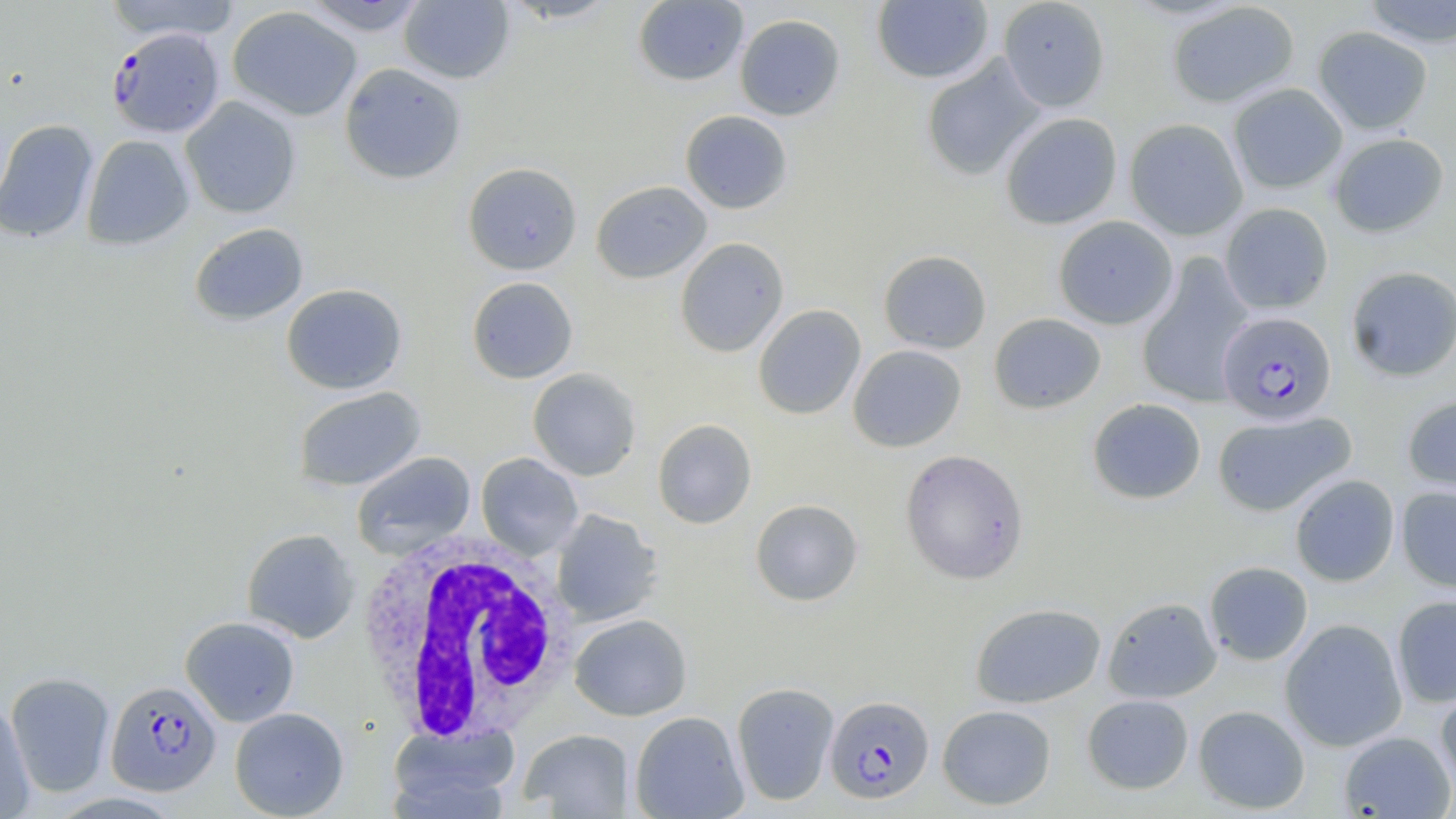
Approximate bounding boxes as (x1, y1, x2, y2) in pixels. Uninfected red blood cell locations: (103, 0, 242, 41), (296, 0, 432, 36), (998, 0, 1111, 112), (399, 1, 514, 85), (500, 1, 621, 24), (632, 1, 748, 87), (872, 1, 994, 84), (1166, 1, 1300, 108), (1359, 1, 1456, 48), (227, 6, 362, 121), (735, 14, 845, 121), (1312, 26, 1433, 134), (920, 54, 1046, 181), (339, 62, 467, 184), (1227, 83, 1347, 195), (180, 96, 302, 219), (679, 110, 793, 214), (999, 112, 1123, 230), (1124, 118, 1248, 240), (0, 119, 98, 243), (1328, 132, 1449, 238), (81, 134, 195, 251), (462, 162, 582, 275), (591, 180, 712, 284), (1220, 203, 1334, 314), (1053, 215, 1178, 330), (189, 222, 308, 326), (674, 237, 789, 357), (878, 250, 992, 354), (1136, 255, 1255, 408), (1345, 266, 1456, 381), (466, 277, 578, 383), (281, 283, 408, 395), (753, 304, 866, 420), (989, 312, 1106, 414), (848, 345, 967, 452), (527, 368, 641, 481), (292, 386, 427, 491), (1402, 394, 1456, 498), (1087, 398, 1206, 504), (1212, 411, 1356, 517), (652, 419, 757, 529), (899, 449, 1029, 585), (351, 451, 476, 559), (476, 453, 583, 559), (1290, 473, 1400, 587), (1396, 486, 1456, 593), (750, 498, 864, 606), (550, 509, 664, 626), (241, 528, 359, 644), (1204, 561, 1313, 666), (1391, 594, 1456, 708), (1102, 597, 1222, 703), (970, 602, 1105, 708), (569, 614, 692, 721), (180, 616, 300, 726), (1280, 618, 1407, 752), (5, 672, 115, 797), (731, 681, 839, 806), (1435, 683, 1456, 794), (1082, 693, 1194, 795), (0, 700, 36, 817), (937, 705, 1057, 810), (1192, 705, 1311, 813), (230, 707, 349, 818), (629, 711, 749, 818), (389, 722, 519, 817), (519, 729, 634, 817), (1338, 730, 1455, 818). White blood cell locations: (353, 530, 576, 746). Plasmodium falciparum-infected red blood cell locations: (107, 27, 226, 138), (1217, 311, 1337, 425), (105, 680, 221, 797), (824, 695, 935, 804). Slide-level diagnosis: Plasmodium falciparum. Light microscopy. Thin blood film. May-Grünwald-Giemsa-stained preparation. Image is 1456×819 pixels. Single field of view. 1000x magnification.